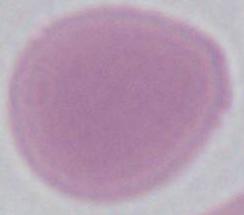
Photomicrograph. A red blood cell is seen. Captured at 1000x magnification.